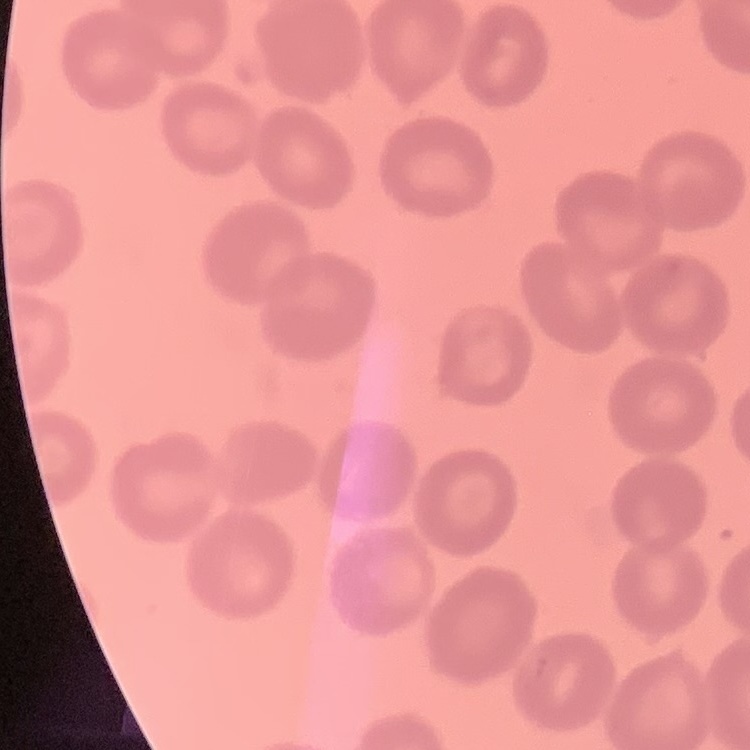
The red blood cells show no rouleaux formation. Square crop of a larger photomicrograph. Stained with either Field's or Giemsa. Thin blood film.